Describe the morphology of the red blood cells.
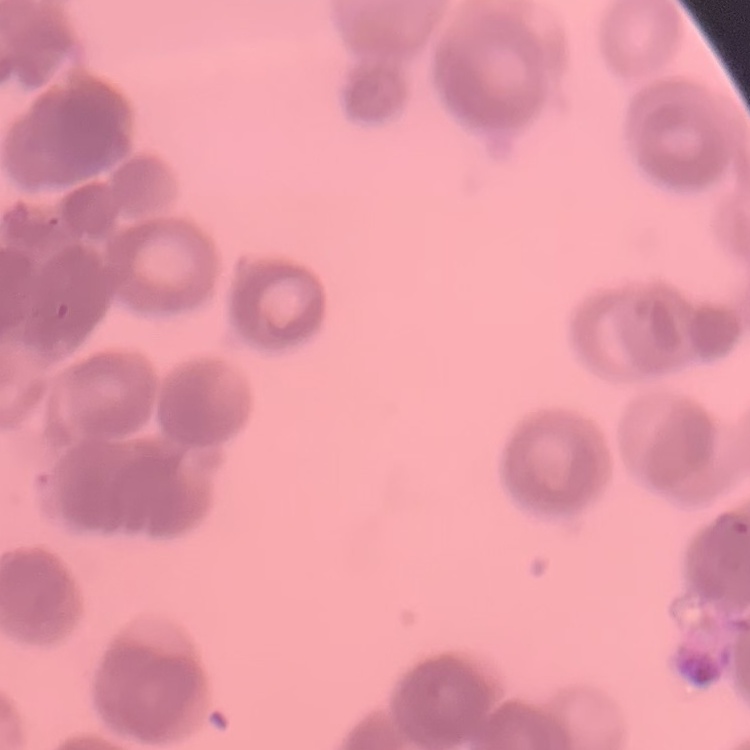
Rouleaux formation.

{
  "preparation": "thin blood film",
  "stain": "Field's or Giemsa",
  "image_type": "one tile cut from a larger photomicrograph"
}